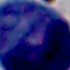

Summary:
  - Modality: micrograph
  - Magnification: 1000x
  - Identification: leukocyte